Assess for malaria.
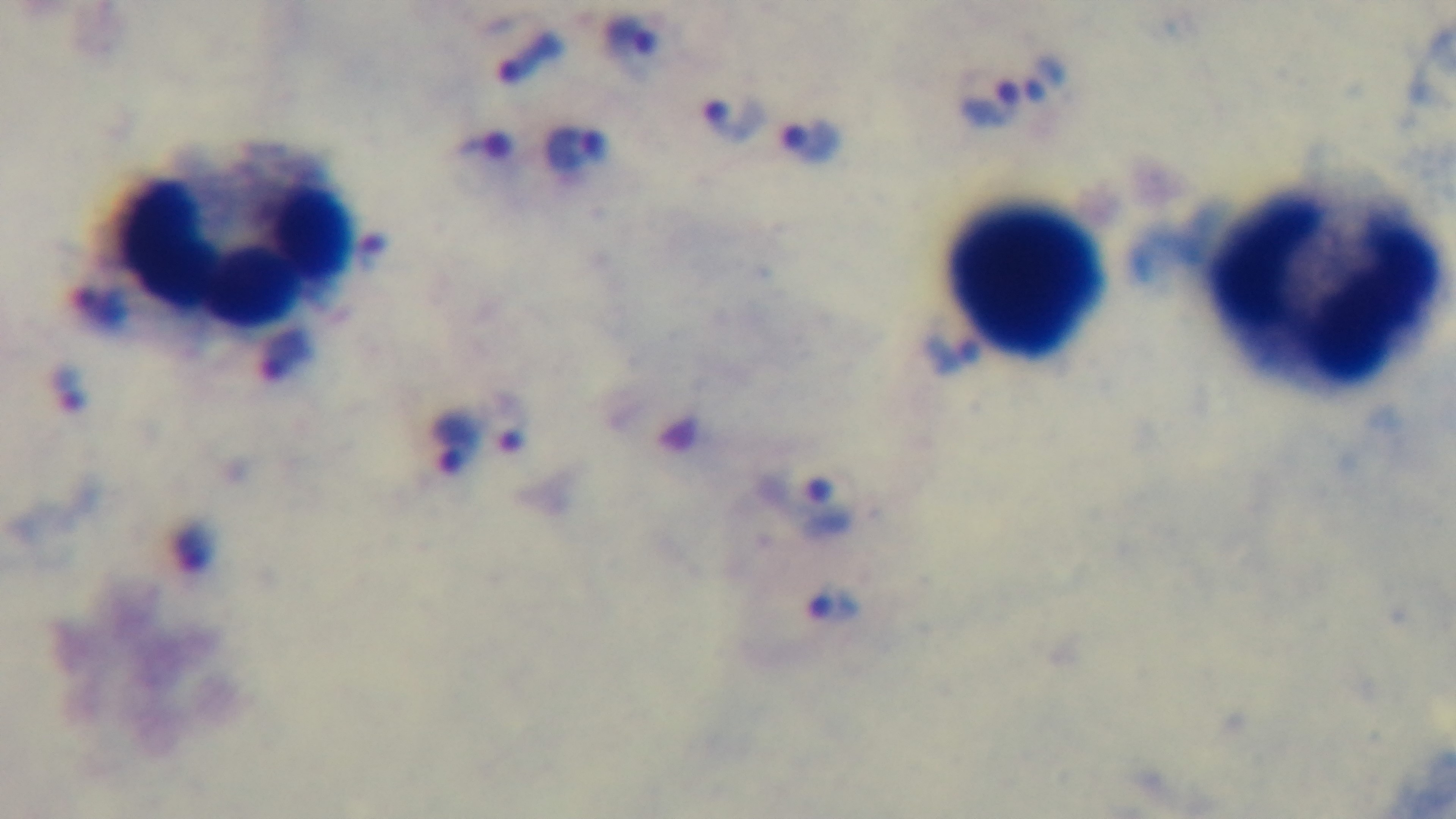

Positive.

preparation = thick blood film
stain = Giemsa
modality = light microscopy
field of view = one from the slide
capture = mounted 4K digital camera
objective = 100x oil immersion